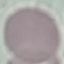
Summary:
  - Malaria status: uninfected
  - Image type: cell patch, automatically extracted from a larger field of view and resized to 64 × 64 pixels
  - Capture: smartphone through the microscope eyepiece
  - Preparation: thin blood film
  - Stain: Giemsa